State which parasite is depicted.
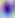

Toxoplasma gondii.

Summary:
  - Magnification: 400x
  - Modality: micrograph